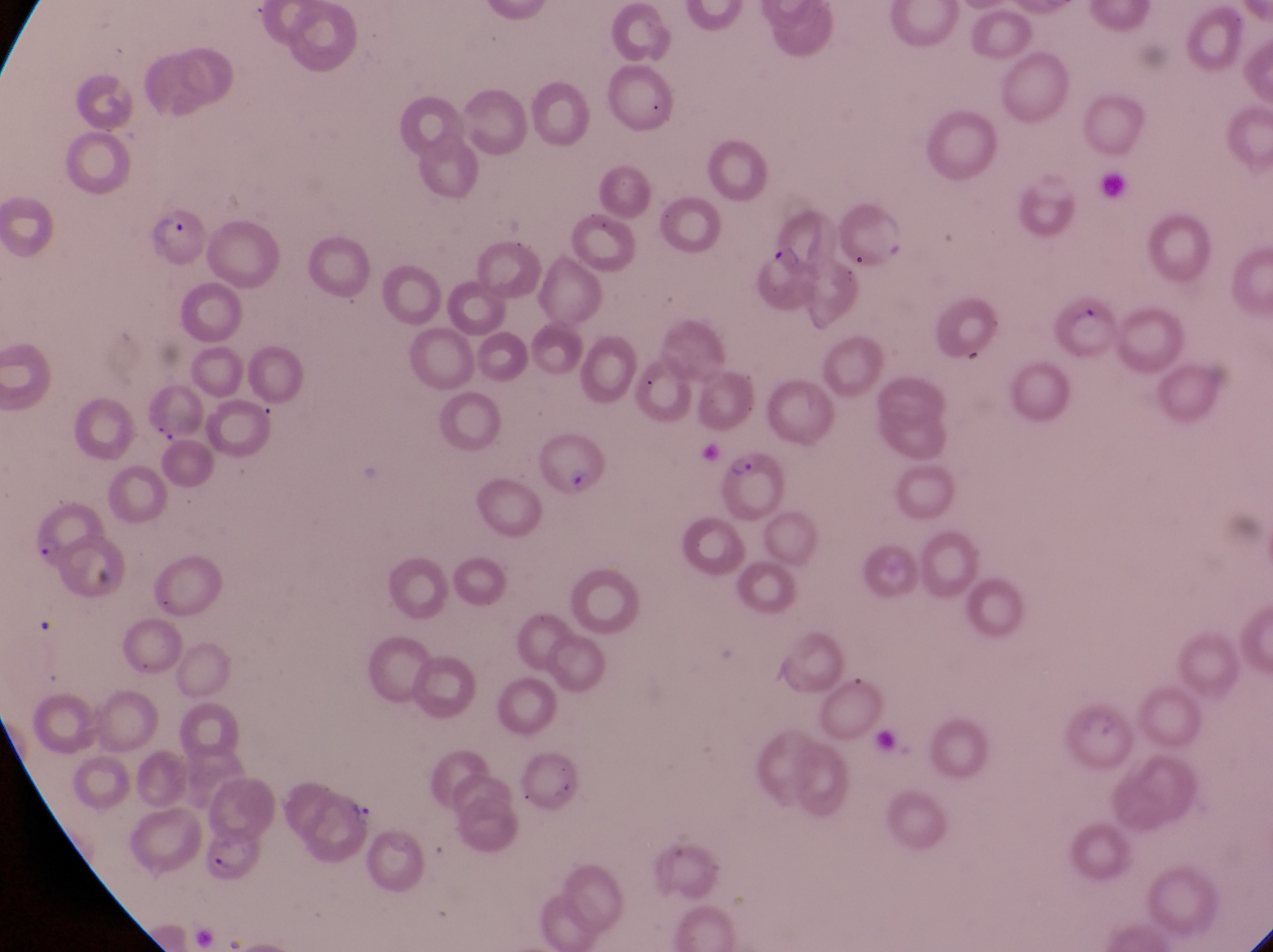

magnification = 1000x
country = Uganda
trophozoite locations = approximate bounding boxes as (left, top, right, bottom) in pixels: (345, 796, 377, 831)
field of view = single
capture = smartphone photograph through the eyepiece of an Olympus CX-23 microscope
parasitised red blood cell locations = approximate bounding boxes as (left, top, right, bottom) in pixels: (764, 205, 827, 273), (148, 209, 213, 272), (836, 210, 911, 278), (1058, 292, 1120, 364), (537, 440, 614, 510), (721, 445, 788, 520), (20, 484, 102, 567), (1055, 696, 1133, 771)
image size = 1273×952 pixels
preparation = thin blood smear
artifact (platelet-like body, stain precipitate, or debris) locations = approximate bounding boxes as (left, top, right, bottom) in pixels: (145, 417, 182, 449), (95, 562, 132, 599), (876, 726, 909, 754), (207, 856, 239, 878)